Point out each Plasmodium parasite.
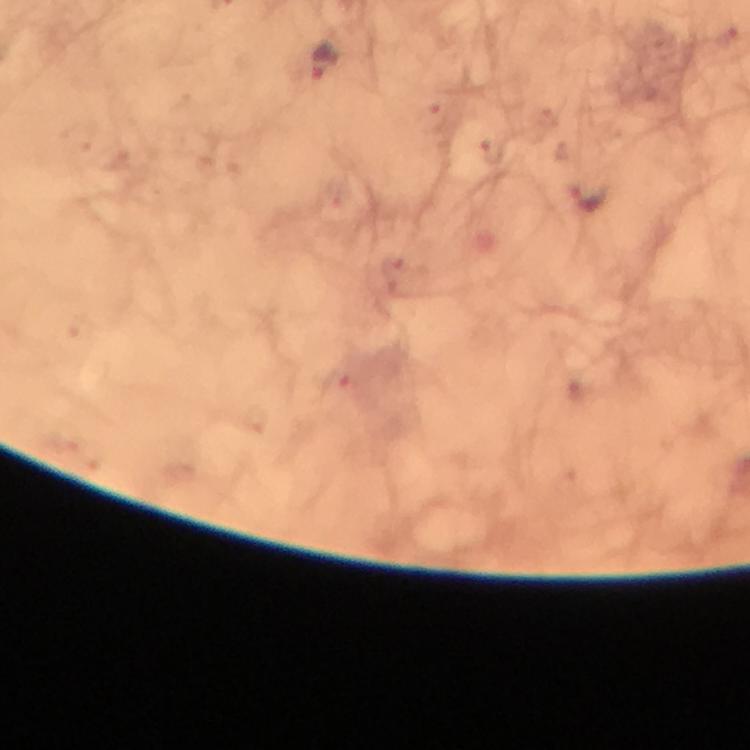
Approximate centers as {x, y} in pixels.
Plasmodium parasites: {323, 63}, {587, 197}.

Immersion oil applied. Image is 750×750 pixels. From a malaria diagnostic workup. At 100x magnification. Photographed through the microscope with a smartphone camera. Cropped region of a single field of view. Thick blood smear. Giemsa stain.